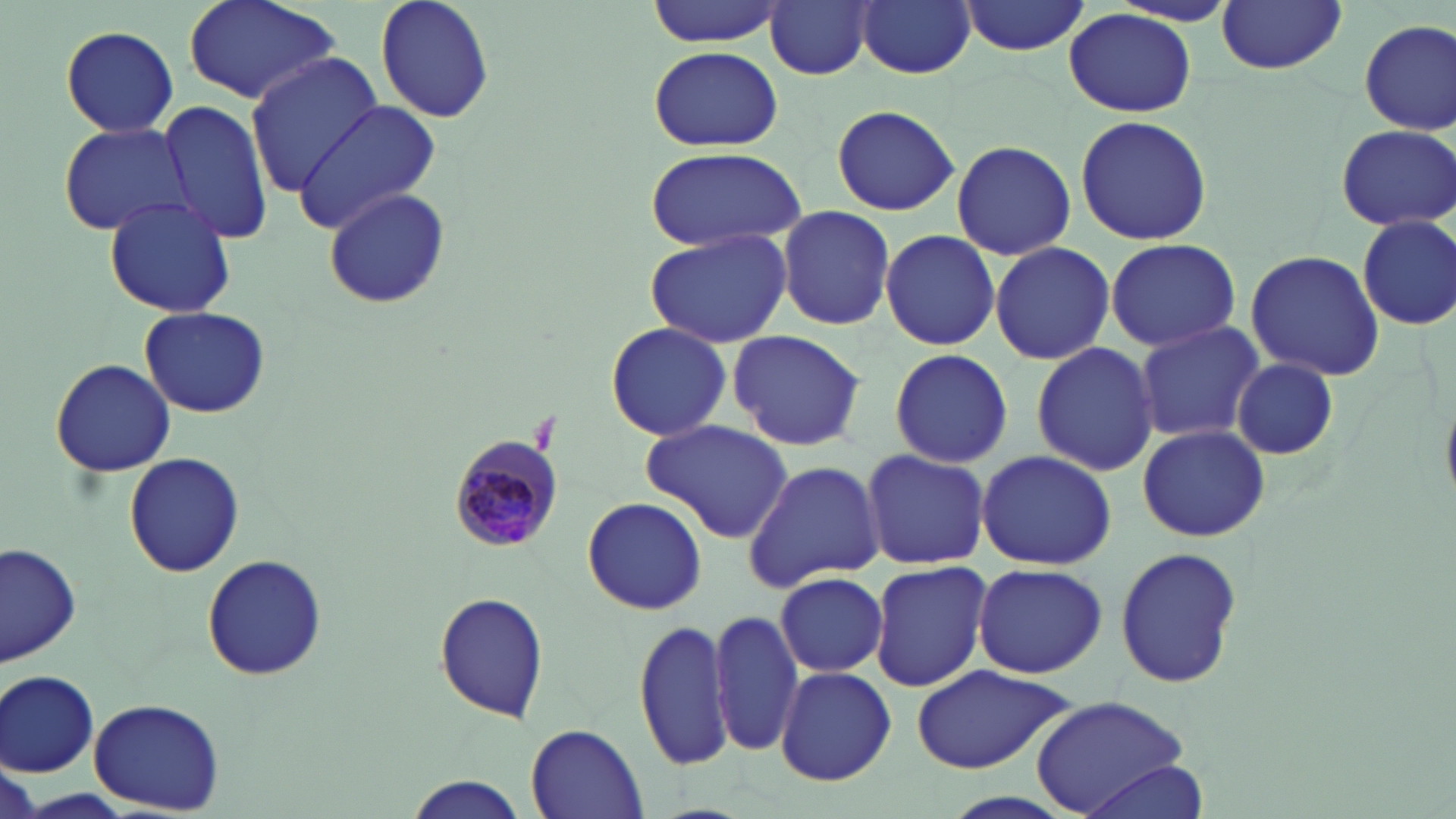

{
  "plasmodium_malariae_infected_red_blood_cell_locations": "approximate bounding boxes as named x1/y1/x2/y2 corners in pixels: (x1=447, y1=435, x2=566, y2=553)",
  "slide_level_diagnosis": "Plasmodium malariae",
  "preparation": "thin blood smear",
  "magnification": "1000x",
  "uninfected_red_blood_cell_locations": "approximate bounding boxes as named x1/y1/x2/y2 corners in pixels: (x1=182, y1=0, x2=344, y2=108), (x1=375, y1=0, x2=495, y2=124), (x1=645, y1=0, x2=786, y2=46), (x1=765, y1=0, x2=874, y2=81), (x1=857, y1=0, x2=975, y2=79), (x1=959, y1=0, x2=1093, y2=55), (x1=1215, y1=1, x2=1347, y2=75), (x1=1064, y1=8, x2=1198, y2=118), (x1=1357, y1=18, x2=1456, y2=134), (x1=59, y1=25, x2=180, y2=136), (x1=648, y1=45, x2=783, y2=153), (x1=243, y1=52, x2=381, y2=196), (x1=159, y1=97, x2=274, y2=247), (x1=291, y1=99, x2=445, y2=230), (x1=832, y1=104, x2=961, y2=217), (x1=1074, y1=114, x2=1212, y2=244), (x1=58, y1=122, x2=193, y2=236), (x1=1335, y1=125, x2=1454, y2=231), (x1=950, y1=138, x2=1076, y2=262), (x1=644, y1=147, x2=808, y2=252), (x1=322, y1=187, x2=450, y2=310), (x1=102, y1=195, x2=237, y2=317), (x1=775, y1=207, x2=896, y2=329), (x1=1354, y1=212, x2=1456, y2=330), (x1=643, y1=226, x2=794, y2=348), (x1=880, y1=228, x2=999, y2=352), (x1=1104, y1=238, x2=1241, y2=351), (x1=989, y1=240, x2=1116, y2=365), (x1=1244, y1=249, x2=1387, y2=381), (x1=139, y1=306, x2=270, y2=418), (x1=1132, y1=320, x2=1267, y2=445), (x1=602, y1=322, x2=734, y2=442), (x1=728, y1=328, x2=867, y2=452), (x1=1030, y1=342, x2=1161, y2=476), (x1=887, y1=349, x2=1012, y2=468), (x1=49, y1=357, x2=178, y2=479), (x1=1232, y1=358, x2=1340, y2=459), (x1=640, y1=419, x2=793, y2=543), (x1=1136, y1=424, x2=1272, y2=540), (x1=859, y1=447, x2=990, y2=571), (x1=974, y1=450, x2=1117, y2=570), (x1=122, y1=453, x2=246, y2=577), (x1=742, y1=458, x2=884, y2=590), (x1=583, y1=498, x2=706, y2=614), (x1=2, y1=541, x2=82, y2=668), (x1=1115, y1=545, x2=1243, y2=691), (x1=201, y1=554, x2=327, y2=682), (x1=869, y1=559, x2=991, y2=691), (x1=970, y1=560, x2=1108, y2=679), (x1=773, y1=570, x2=888, y2=677), (x1=434, y1=592, x2=551, y2=722), (x1=711, y1=607, x2=802, y2=756), (x1=632, y1=618, x2=733, y2=771), (x1=911, y1=664, x2=1077, y2=774), (x1=776, y1=666, x2=895, y2=785), (x1=1, y1=671, x2=100, y2=776), (x1=87, y1=697, x2=225, y2=813), (x1=1031, y1=697, x2=1196, y2=816), (x1=525, y1=725, x2=648, y2=817), (x1=1074, y1=760, x2=1209, y2=817), (x1=403, y1=776, x2=526, y2=817)",
  "field_of_view": "one of a larger specimen",
  "modality": "light microscopy",
  "stain": "May-Grünwald-Giemsa",
  "image_size": "1456×819 pixels"
}